Assess this cell for malaria.
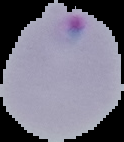
It is parasitized.

Summary:
  - Image size: 124×142 pixels
  - Preparation: thin blood film
  - Image type: cell region segmented out of the field of view; surrounding area masked to black